Comment on the morphology of the red blood cells.
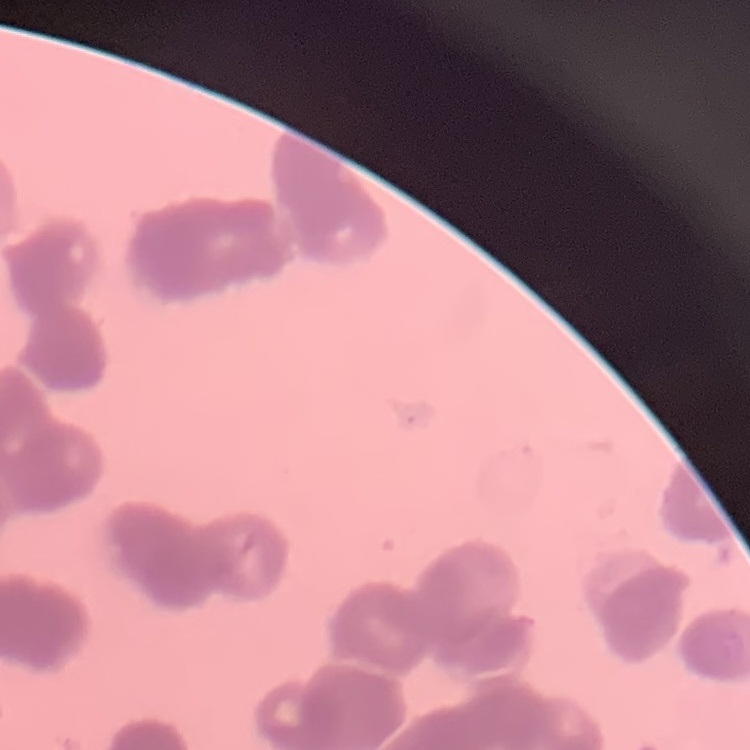
Rouleaux formation.

Thin blood smear. Field's or Giemsa stain. One tile cut from a larger photomicrograph.